Classify this cell by malaria status.
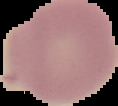
Uninfected.

image_size: 118×106 pixels
image_type: segmented cell region with the area outside set to black
preparation: thin blood film